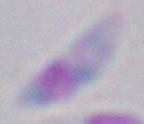

identification = Toxoplasma gondii
magnification = 1000x
modality = photomicrograph